Outline platelets.
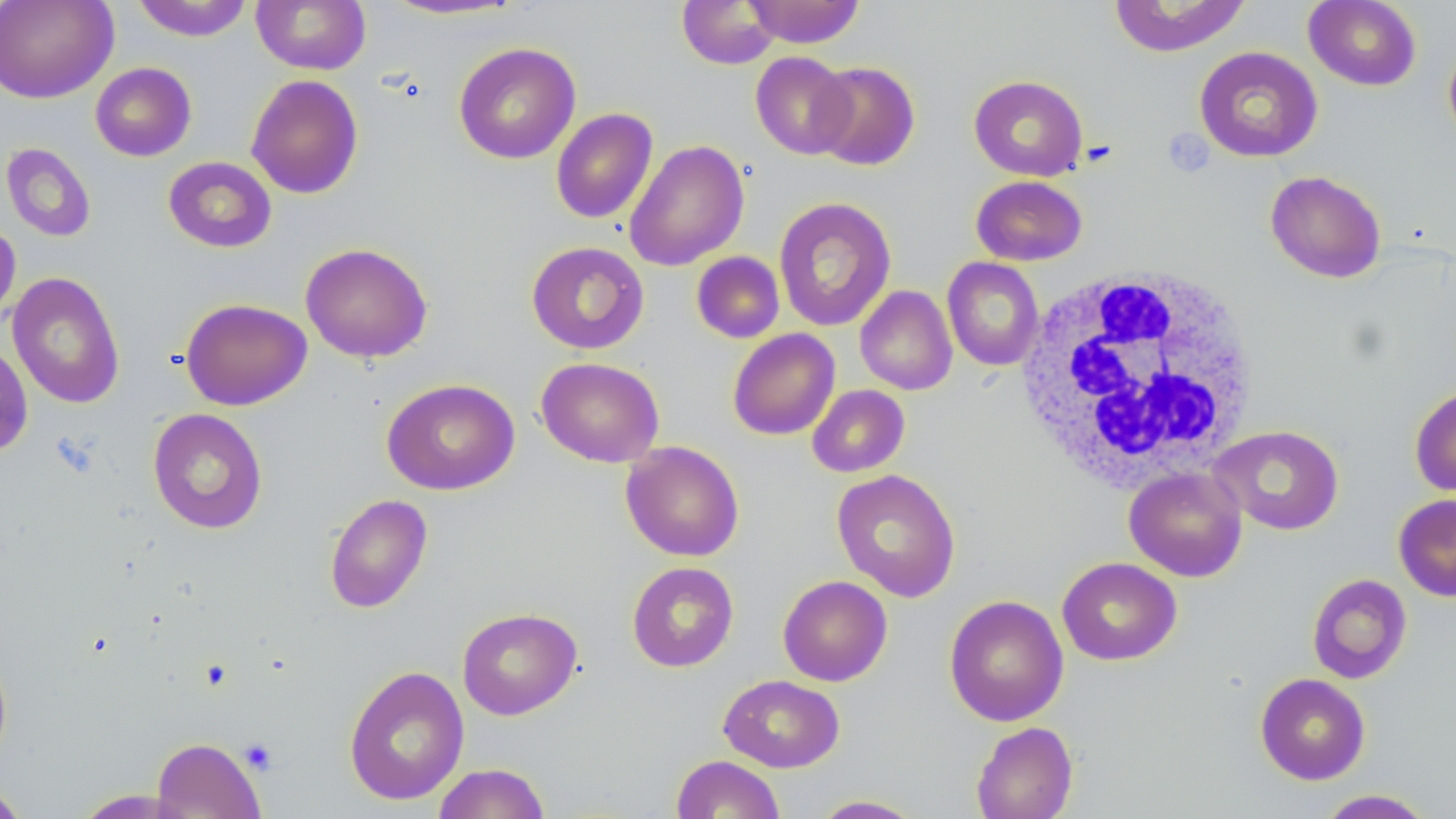

Approximate bounding boxes as (x1, y1, x2, y2) in pixels.
Platelets: (1162, 128, 1214, 175), (239, 738, 278, 775).

Summary:
  - Uninfected red blood cell locations: (0, 0, 117, 104), (131, 0, 255, 41), (251, 0, 372, 74), (377, 0, 529, 21), (677, 0, 781, 69), (742, 0, 866, 48), (1108, 0, 1250, 56), (1303, 0, 1421, 91), (1443, 37, 1456, 151), (454, 42, 581, 164), (1194, 46, 1322, 162), (750, 52, 855, 159), (810, 61, 920, 170), (90, 62, 196, 161), (245, 74, 364, 199), (969, 75, 1088, 180), (551, 108, 658, 224), (624, 139, 749, 271), (1, 143, 96, 242), (163, 156, 277, 253), (1265, 170, 1386, 283), (971, 175, 1087, 265), (773, 197, 896, 332), (0, 218, 21, 329), (525, 241, 649, 354), (299, 242, 433, 363), (691, 252, 785, 343), (943, 257, 1044, 371), (7, 271, 125, 409), (855, 285, 957, 395), (180, 298, 312, 410), (727, 328, 840, 440), (536, 357, 665, 468), (381, 378, 520, 495), (1409, 384, 1456, 498), (807, 385, 910, 478), (147, 408, 268, 534), (1210, 425, 1345, 535), (620, 440, 744, 561), (1124, 466, 1248, 582), (831, 468, 961, 602), (324, 494, 433, 613), (1393, 494, 1456, 601), (1057, 557, 1182, 666), (626, 561, 740, 672), (1307, 573, 1412, 684), (777, 575, 893, 686), (944, 595, 1069, 726), (456, 607, 583, 720), (0, 645, 13, 768), (343, 664, 469, 806), (1255, 672, 1371, 785), (718, 674, 845, 772), (971, 722, 1078, 819), (151, 737, 266, 819), (671, 755, 785, 818), (432, 762, 551, 819), (0, 780, 32, 819), (72, 789, 190, 818), (1315, 789, 1436, 818), (809, 795, 925, 818)
  - White blood cell locations: (1014, 266, 1262, 493)
  - Slide-level diagnosis: negative for blood parasites
  - Modality: light microscopy
  - Preparation: thin blood smear
  - Image size: 1456×819 pixels
  - Stain: May-Grünwald-Giemsa
  - Magnification: 1000x
  - Field of view: one of a larger specimen